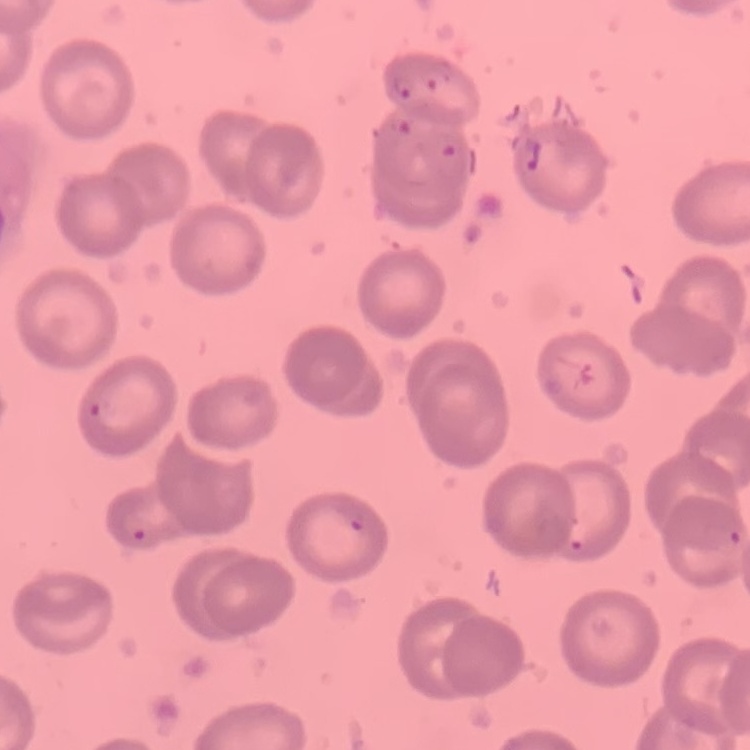
erythrocyte morphology = no rouleaux formation
preparation = thin blood smear
stain = Field's or Giemsa
image type = one tile cut from a larger photomicrograph